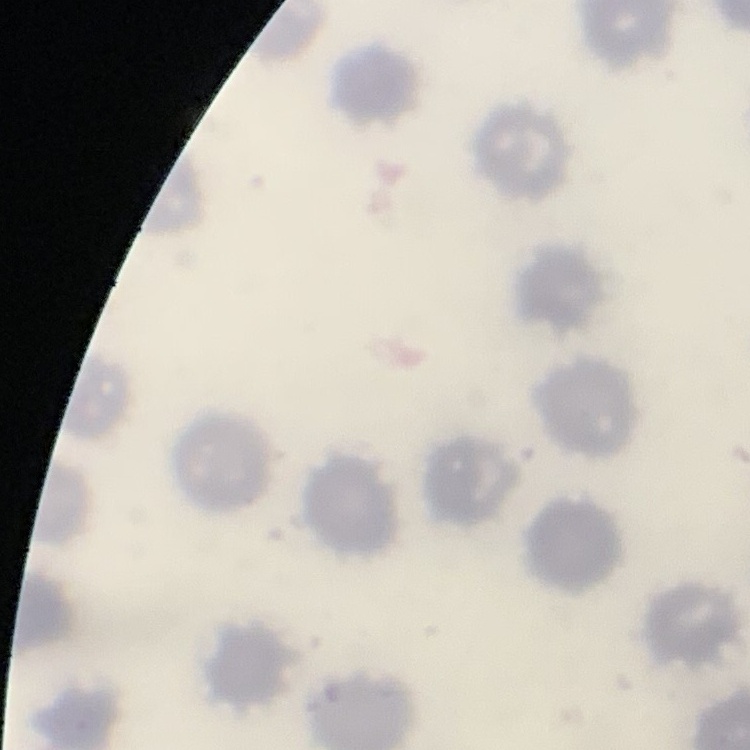
The erythrocytes show no rouleaux formation. Thin blood smear. Stained with either Field's or Giemsa. One tile cut from a larger photomicrograph.